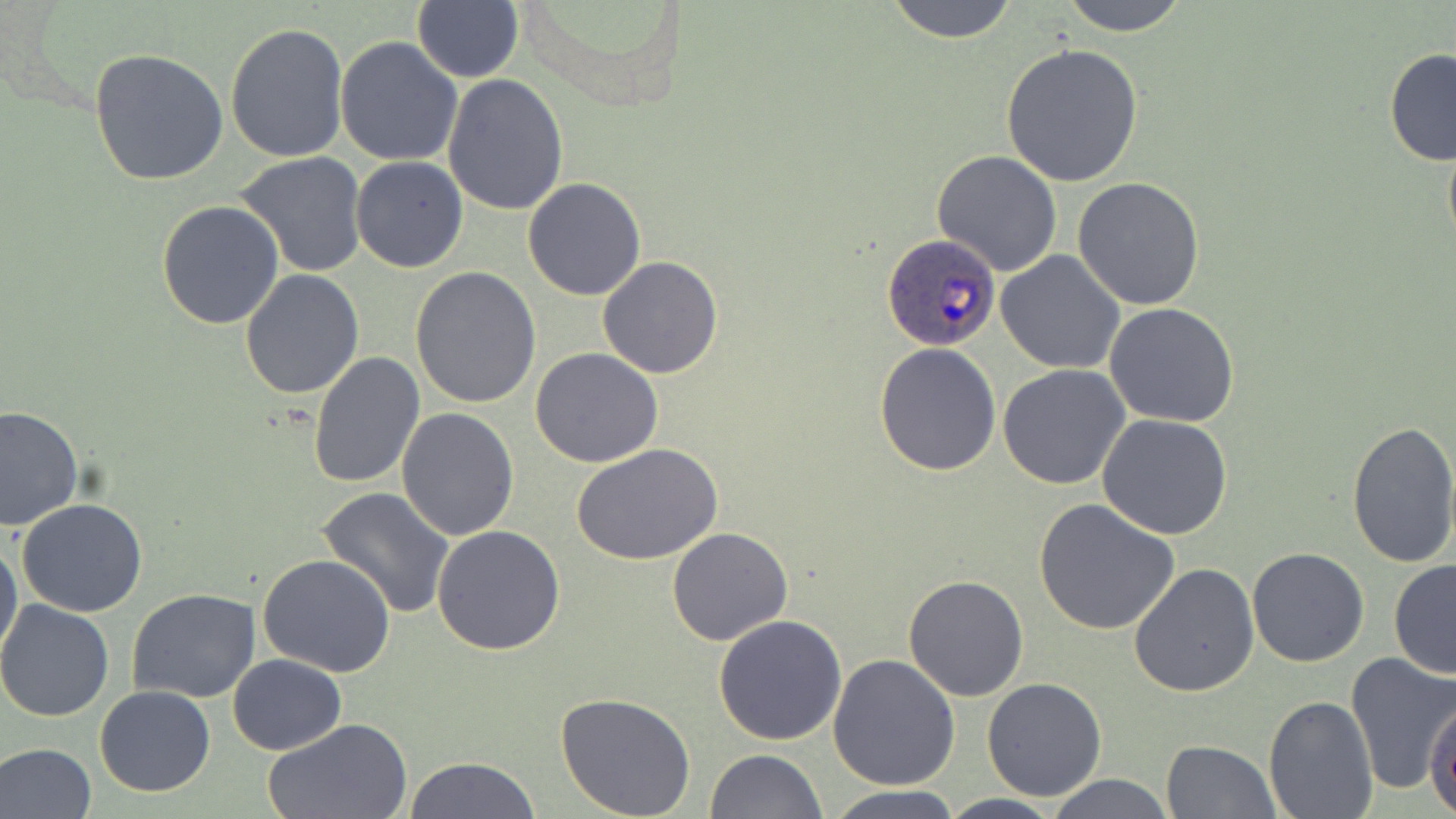 Approximate bounding boxes as [x1, y1, x2, y2] in pixels. Plasmodium ovale-infected red blood cell locations: [883, 232, 1000, 349]. Uninfected red blood cell locations: [883, 0, 1022, 44], [1057, 0, 1193, 34], [412, 1, 524, 84], [225, 22, 348, 162], [335, 38, 462, 166], [1000, 43, 1144, 186], [88, 47, 229, 186], [1383, 49, 1456, 167], [441, 74, 568, 216], [1442, 125, 1456, 261], [932, 151, 1063, 276], [235, 152, 369, 279], [350, 157, 468, 272], [1073, 176, 1206, 310], [522, 177, 648, 300], [156, 200, 284, 329], [996, 251, 1127, 374], [597, 256, 724, 378], [409, 266, 542, 409], [239, 268, 365, 398], [1103, 303, 1242, 428], [874, 343, 1002, 477], [530, 347, 662, 468], [309, 350, 425, 491], [998, 364, 1131, 489], [0, 406, 84, 532], [397, 407, 521, 541], [1097, 413, 1234, 541], [1345, 417, 1456, 567], [574, 444, 723, 567], [317, 487, 456, 618], [1032, 498, 1180, 635], [16, 499, 149, 619], [431, 524, 566, 656], [666, 527, 795, 646], [0, 534, 23, 667], [1245, 547, 1369, 667], [257, 554, 397, 677], [1389, 559, 1456, 680], [1128, 564, 1259, 699], [903, 573, 1031, 702], [127, 588, 259, 703], [0, 600, 113, 722], [714, 613, 846, 744], [227, 653, 347, 755], [829, 653, 961, 791], [1345, 654, 1456, 794], [982, 678, 1107, 802], [95, 686, 216, 798], [554, 691, 697, 818], [1263, 696, 1377, 817], [1426, 698, 1456, 817], [262, 717, 417, 819], [1162, 740, 1280, 819], [0, 743, 98, 818], [704, 749, 828, 818], [404, 756, 540, 819], [1045, 774, 1175, 818], [824, 786, 968, 819], [934, 794, 1067, 819]. Slide-level diagnosis: Plasmodium ovale. Image is 1456×819 pixels. Thin blood film. May-Grünwald-Giemsa stain. Single field of view. Optical microscopy. 1000x magnification.